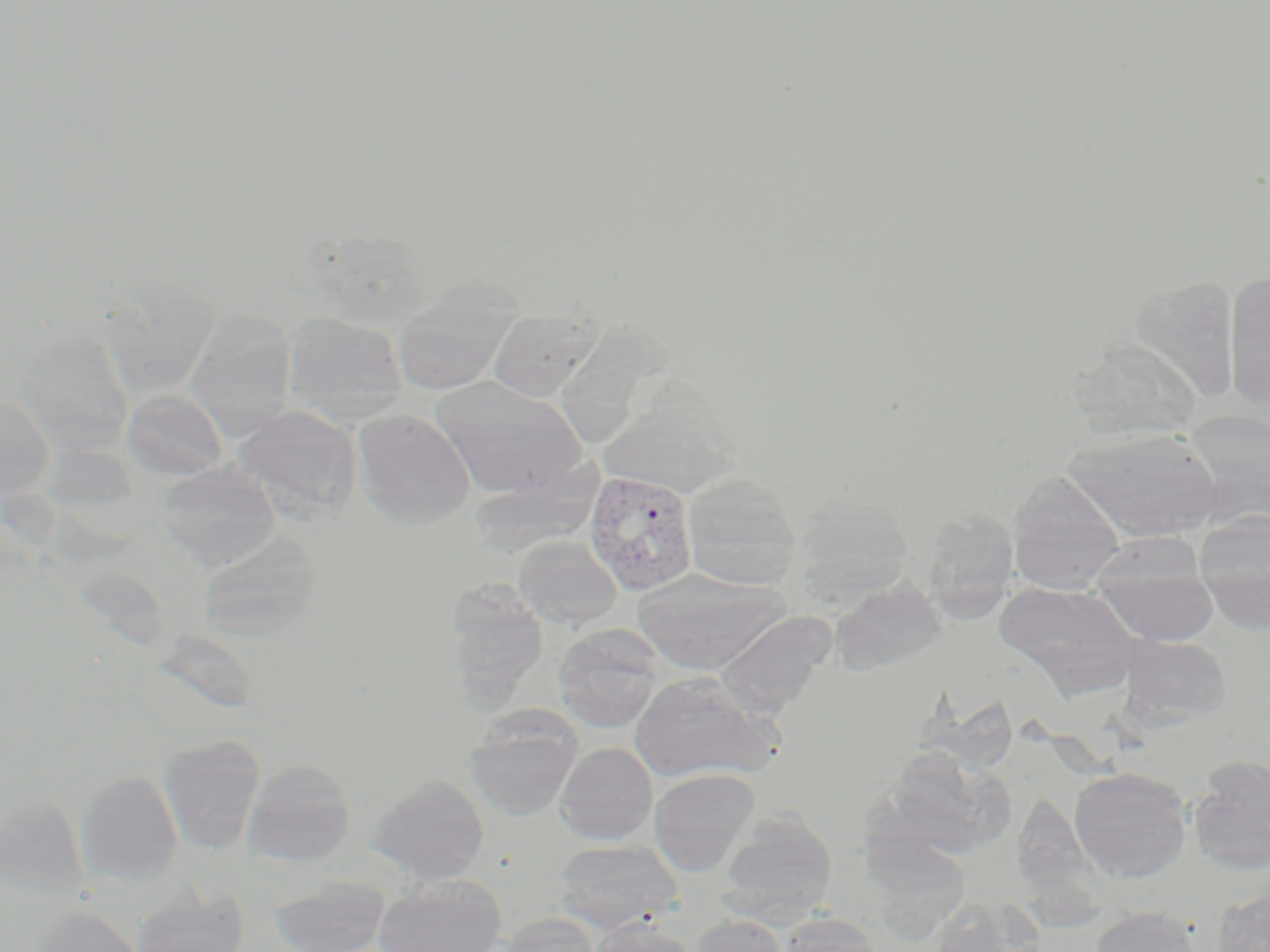

Approximate bounding boxes as (x1, y1, x2, y2) in pixels. Plasmodium vivax-infected red blood cell locations: (584, 469, 699, 596). Uninfected red blood cell locations: (1224, 270, 1270, 411), (1132, 274, 1239, 403), (393, 282, 519, 397), (487, 308, 601, 402), (184, 310, 298, 437), (282, 312, 408, 423), (15, 328, 136, 456), (1070, 339, 1202, 441), (432, 376, 586, 499), (606, 376, 758, 501), (123, 389, 229, 481), (0, 393, 55, 499), (231, 404, 362, 522), (353, 408, 475, 528), (1181, 409, 1270, 528), (1064, 426, 1222, 541), (157, 462, 281, 569), (470, 466, 602, 556), (682, 472, 803, 589), (1006, 473, 1127, 594), (792, 497, 914, 603), (920, 507, 1020, 620), (1193, 511, 1270, 631), (198, 532, 320, 638), (514, 535, 622, 627), (1089, 536, 1218, 645), (632, 569, 788, 674), (830, 577, 946, 674), (994, 580, 1143, 695), (446, 584, 550, 713), (715, 610, 838, 718), (553, 626, 664, 733), (1116, 634, 1231, 728), (631, 671, 776, 782), (465, 707, 581, 820), (158, 734, 265, 854), (555, 742, 658, 844), (878, 749, 1016, 859), (1188, 756, 1270, 875), (243, 758, 356, 866), (1069, 767, 1192, 882), (648, 768, 759, 876), (77, 770, 183, 884), (370, 773, 490, 883), (1010, 791, 1128, 927), (1, 793, 90, 899), (718, 812, 837, 925), (861, 833, 971, 938), (553, 838, 683, 933), (374, 873, 507, 952), (269, 875, 390, 952), (1210, 885, 1270, 951), (132, 888, 250, 952), (927, 896, 1044, 951), (31, 905, 144, 952), (1090, 905, 1204, 952), (497, 914, 602, 952), (689, 914, 788, 952), (778, 914, 886, 952), (590, 918, 697, 952). Slide-level diagnosis: Plasmodium vivax. May-Grünwald-Giemsa stain. Captured at 1000x magnification. Light microscopy. Thin blood smear. Image is 1270×952 pixels. One field of a larger specimen.